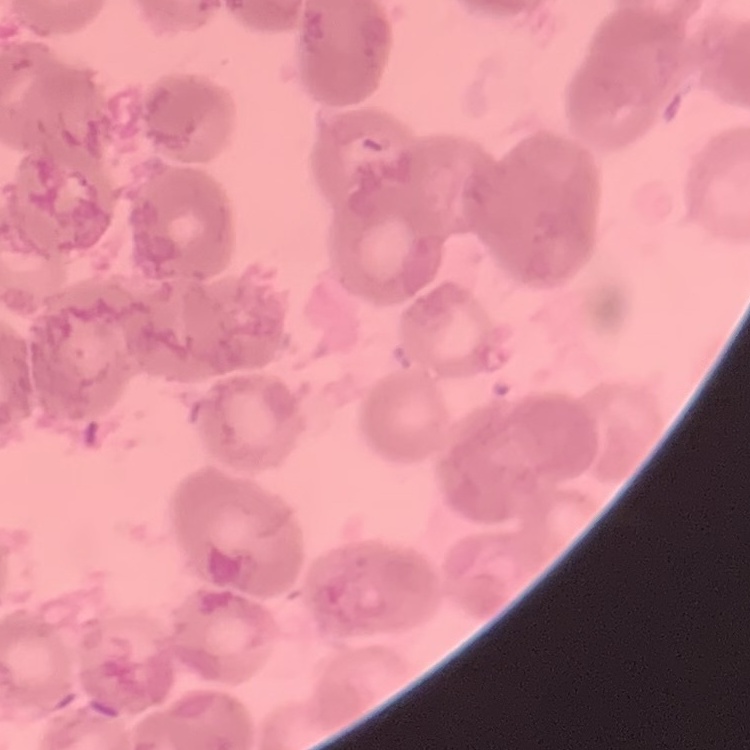 The red blood cells exhibit rouleaux formation. Square crop of a larger photomicrograph. Thin blood film. Stained with either Field's or Giemsa.